Report the malaria status of this cell.
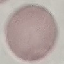

Uninfected.

capture = smartphone camera at the microscope eyepiece
stain = Giemsa
preparation = thin smear
image type = automatically extracted cell patch, resized to 64 × 64 pixels